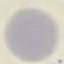

Summary:
  - Malaria status: uninfected
  - Preparation: thin smear
  - Image type: automatically extracted cell patch, resized to 64 × 64 pixels
  - Capture: smartphone camera at the microscope eyepiece
  - Stain: Giemsa